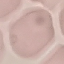

malaria status = uninfected
stain = Giemsa
capture = smartphone through the microscope eyepiece
image type = cell patch, automatically extracted from a larger field of view and resized to 64 × 64 pixels
preparation = thin blood smear